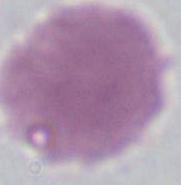

Micrograph. An erythrocyte is seen. Captured at 1000x magnification.